Outline each Plasmodium vivax-infected red blood cell.
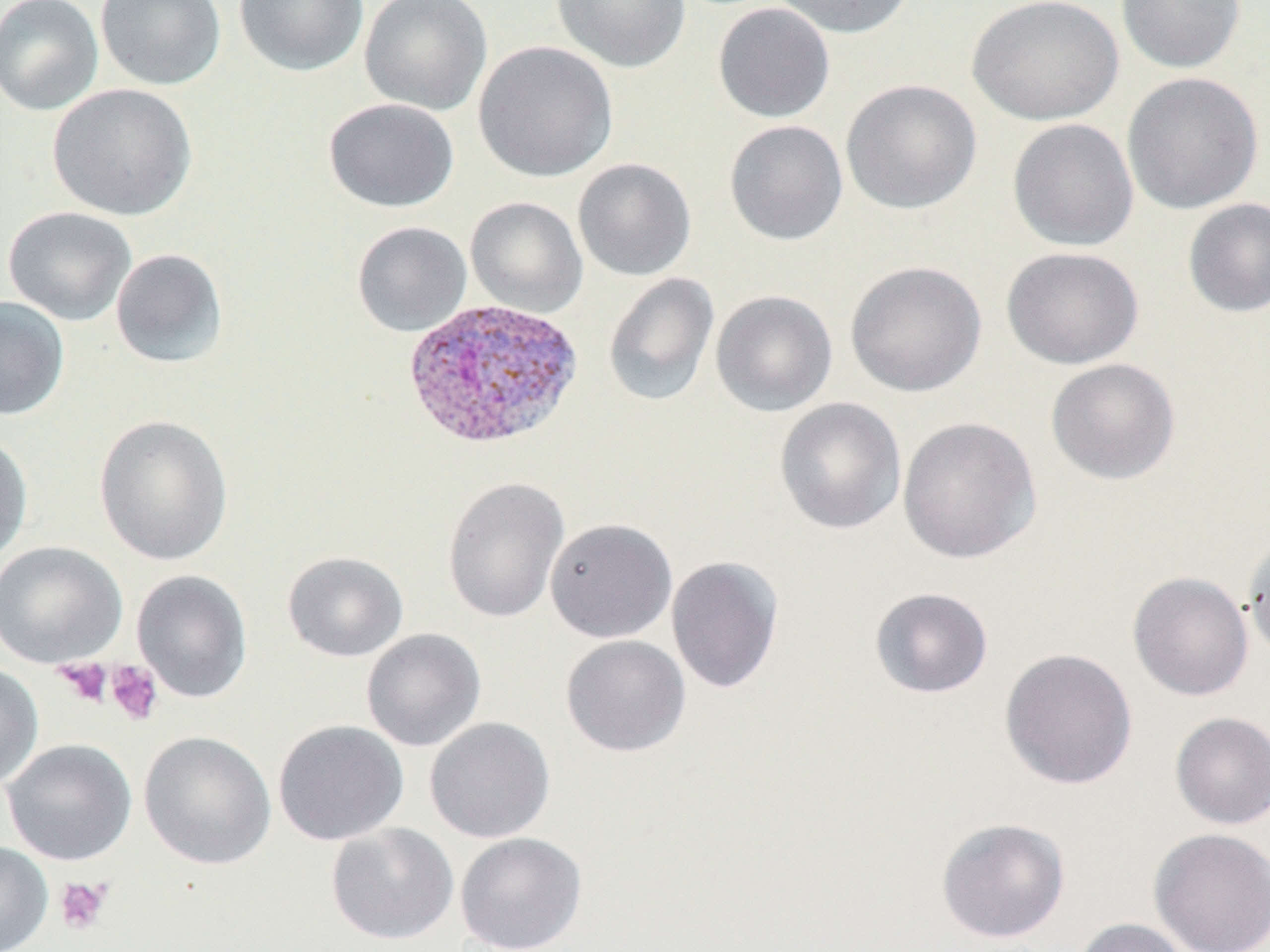

Approximate bounding boxes as (x1,y1)-(x2,y2) corner pairs in pixels.
Plasmodium vivax-infected red blood cells: (401,299)-(584,452).

Summary:
  - Uninfected red blood cell locations: (0,0)-(103,116), (96,0)-(226,91), (233,0)-(370,77), (359,0)-(492,116), (551,0)-(692,73), (769,0)-(916,39), (967,0)-(1123,125), (1116,0)-(1246,74), (712,3)-(835,123), (472,40)-(618,183), (1121,71)-(1264,215), (841,78)-(982,215), (47,83)-(197,221), (324,98)-(459,212), (1007,118)-(1139,251), (724,119)-(848,245), (572,158)-(697,281), (465,196)-(587,318), (1182,197)-(1269,317), (2,206)-(137,325), (351,221)-(472,336), (1001,246)-(1144,369), (110,248)-(229,369), (845,260)-(987,398), (603,272)-(720,407), (710,290)-(837,416), (0,296)-(69,421), (1045,358)-(1181,485), (774,397)-(906,535), (94,413)-(233,565), (897,416)-(1042,564), (0,432)-(33,565), (441,476)-(570,623), (545,518)-(677,643), (1242,531)-(1270,662), (0,541)-(128,668), (282,551)-(408,662), (666,555)-(784,693), (132,570)-(253,703), (1128,572)-(1254,701), (869,587)-(994,698), (361,628)-(487,752), (560,634)-(691,757), (1000,647)-(1138,790), (0,663)-(44,790), (1170,712)-(1270,830), (424,717)-(556,843), (272,719)-(409,846), (138,730)-(276,870), (2,738)-(137,866), (936,817)-(1071,944), (325,822)-(459,945), (1149,828)-(1270,952), (454,832)-(587,952), (0,841)-(53,952), (1071,918)-(1194,952)
  - Platelet locations: (54,659)-(112,707), (105,661)-(164,726), (54,876)-(113,935)
  - Slide-level diagnosis: Plasmodium vivax
  - Magnification: 1000x
  - Field of view: one of a larger specimen
  - Modality: light microscopy
  - Image size: 1270×952 pixels
  - Preparation: thin blood film
  - Stain: May-Grünwald-Giemsa